Locate and identify every blood parasite.
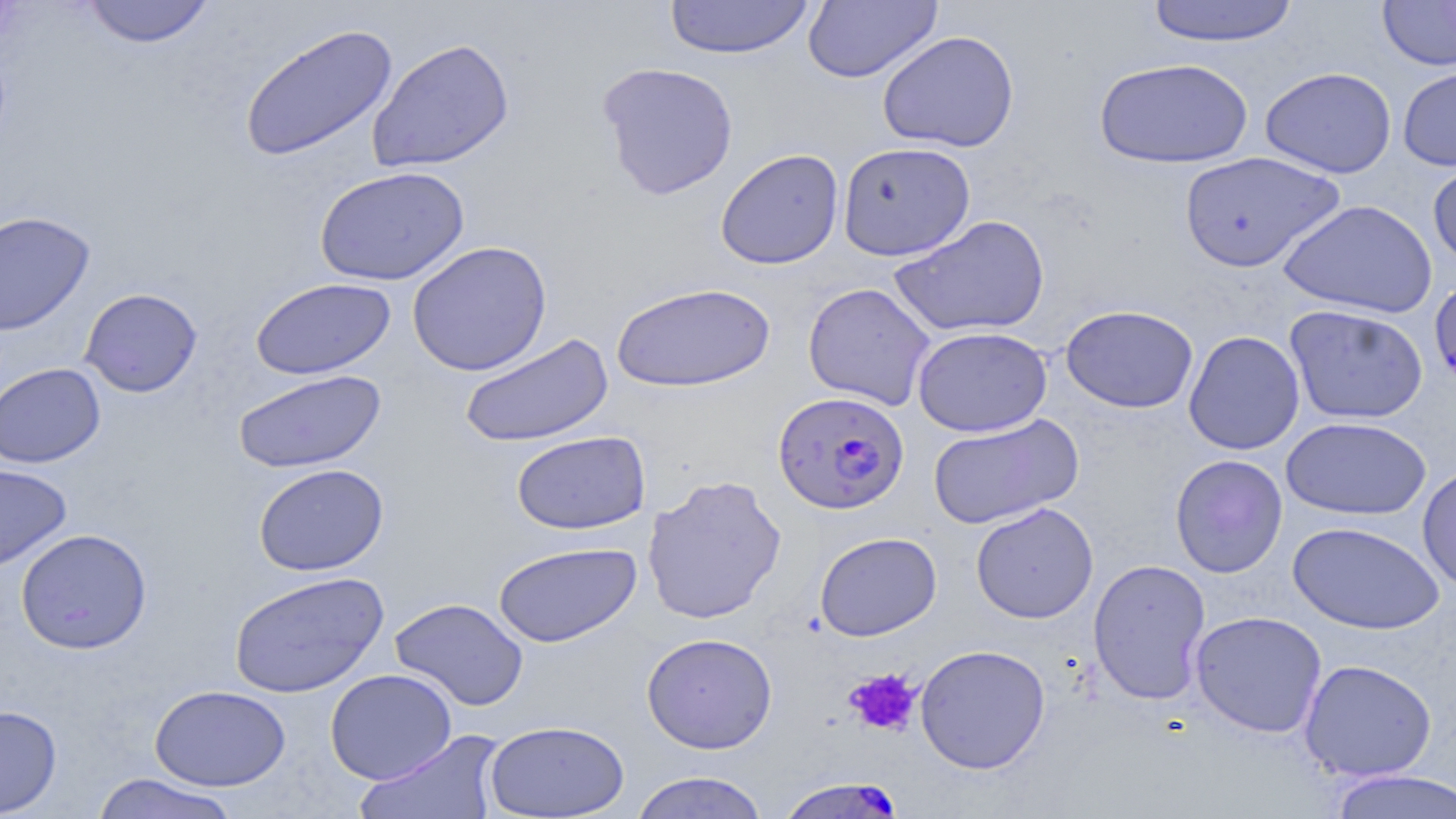

Approximate bounding boxes as [x1, y1, x2, y2] in pixels.
Plasmodium falciparum-infected red blood cells (subset): [773, 390, 910, 514], [777, 775, 907, 818].
No Plasmodium ovale, Plasmodium malariae, Plasmodium vivax, Babesia divergens, or Trypanosoma brucei observed.

Uninfected red blood cell locations (subset): [81, 0, 215, 48], [664, 0, 816, 60], [1145, 0, 1300, 46], [1378, 0, 1456, 70], [802, 1, 943, 83], [237, 22, 399, 163], [877, 30, 1020, 153], [367, 38, 515, 172], [1094, 58, 1254, 169], [597, 61, 739, 201], [1397, 65, 1456, 171], [1260, 66, 1397, 179], [837, 142, 976, 261], [715, 148, 844, 270], [1178, 151, 1344, 273], [1427, 156, 1456, 269], [314, 165, 470, 286], [1278, 198, 1438, 319], [0, 211, 95, 336], [889, 214, 1050, 338], [406, 240, 552, 377], [250, 277, 396, 380], [611, 282, 775, 393], [803, 282, 936, 410], [79, 288, 202, 397], [1060, 304, 1198, 413], [1284, 304, 1429, 425], [912, 327, 1051, 438], [1183, 330, 1305, 455], [458, 332, 614, 447], [0, 362, 105, 468], [232, 369, 386, 473], [927, 413, 1083, 529], [1281, 416, 1432, 521], [510, 431, 651, 535], [1170, 454, 1288, 578], [0, 463, 71, 572], [253, 463, 389, 576], [1417, 465, 1456, 593], [642, 474, 787, 625], [970, 502, 1098, 624], [1287, 520, 1445, 634], [15, 528, 153, 654], [814, 532, 942, 641], [493, 541, 641, 647], [1088, 558, 1212, 706], [229, 571, 389, 698], [390, 597, 529, 711], [1190, 610, 1327, 738], [641, 632, 778, 754], [914, 644, 1051, 774], [1298, 659, 1437, 781], [325, 668, 457, 785], [149, 684, 291, 791], [0, 704, 62, 817], [484, 719, 630, 818], [354, 730, 506, 818], [1326, 769, 1456, 819], [629, 771, 770, 819], [90, 773, 241, 819]. Platelet locations: [844, 667, 921, 736]. Slide-level diagnosis: Plasmodium falciparum. Thin blood smear. Optical microscopy. Image is 1456×819 pixels. 1000x magnification. May-Grünwald-Giemsa stain. Single field of view.